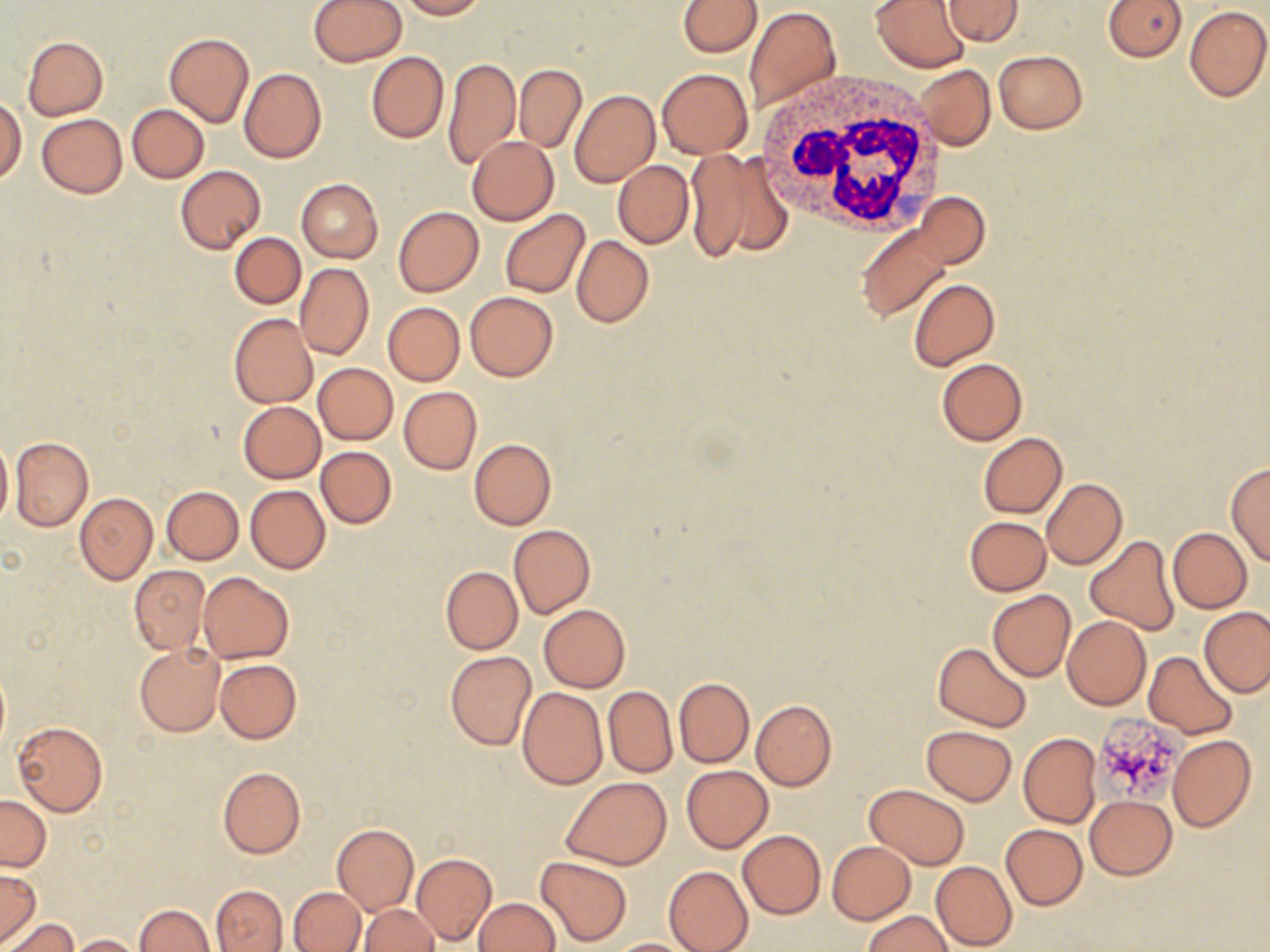
Summary:
  - Coordinate format: approximate bounding boxes as (x1,y1)-(x2,y2) corner pairs in pixels
  - White blood cell locations: (756,73)-(949,237)
  - Platelet locations: (1093,711)-(1186,804)
  - Uninfected red blood cell locations: (308,0)-(408,66), (396,0)-(487,19), (678,0)-(762,56), (872,0)-(970,72), (941,0)-(1024,44), (1103,0)-(1185,60), (684,2)-(831,88), (1184,5)-(1270,102), (744,6)-(841,114), (164,32)-(255,128), (22,36)-(108,120), (994,50)-(1087,133), (367,52)-(449,144), (443,57)-(519,173), (915,64)-(996,151), (513,65)-(586,151), (239,68)-(326,163), (657,69)-(752,159), (568,89)-(658,187), (1,97)-(25,183), (127,104)-(209,182), (37,113)-(127,198), (466,136)-(558,225), (682,147)-(790,264), (613,161)-(694,248), (176,165)-(265,255), (296,178)-(382,263), (913,193)-(989,268), (392,206)-(484,296), (855,206)-(984,322), (500,209)-(590,298), (231,232)-(305,309), (572,236)-(653,327), (296,263)-(374,361), (909,278)-(999,371), (465,292)-(558,382), (383,302)-(464,384), (229,314)-(318,409), (936,359)-(1027,445), (312,362)-(398,445), (400,387)-(482,474), (238,401)-(326,483), (978,432)-(1067,517), (0,435)-(12,527), (10,436)-(93,532), (469,438)-(556,531), (316,446)-(397,529), (1225,462)-(1270,566), (1041,478)-(1126,569), (246,485)-(331,573), (161,486)-(243,564), (74,493)-(158,584), (963,516)-(1051,596), (509,524)-(596,618), (1168,527)-(1252,613), (1085,533)-(1181,635), (129,565)-(210,654), (440,565)-(522,654), (198,571)-(293,663), (987,590)-(1076,681), (538,605)-(630,691), (1200,607)-(1270,698), (1062,616)-(1150,709), (932,643)-(1031,731), (134,645)-(224,737), (446,651)-(536,750), (1144,652)-(1237,739), (215,658)-(300,744), (0,664)-(9,759), (674,677)-(754,768), (604,686)-(677,776), (517,687)-(607,789), (751,700)-(837,790), (12,721)-(107,817), (921,724)-(1017,804), (1019,733)-(1100,827), (1168,735)-(1256,832), (681,765)-(772,852), (216,766)-(305,859), (561,777)-(672,869), (864,784)-(970,869), (1,795)-(51,871), (1086,795)-(1177,880), (331,823)-(419,915), (1000,824)-(1087,910), (737,830)-(826,920), (826,841)-(916,924), (411,852)-(496,946), (534,855)-(633,947), (931,861)-(1017,951), (663,865)-(753,952), (0,868)-(41,944), (210,884)-(288,951), (289,886)-(365,951), (473,898)-(560,951), (134,904)-(214,952), (360,904)-(437,952), (863,912)-(952,952), (5,916)-(77,952), (68,934)-(142,951), (605,938)-(694,951)
  - Slide-level diagnosis: no evidence of blood parasites
  - Magnification: 1000x
  - Image size: 1270×952 pixels
  - Modality: light microscopy
  - Stain: May-Grünwald-Giemsa
  - Preparation: thin blood film
  - Field of view: one of a larger specimen